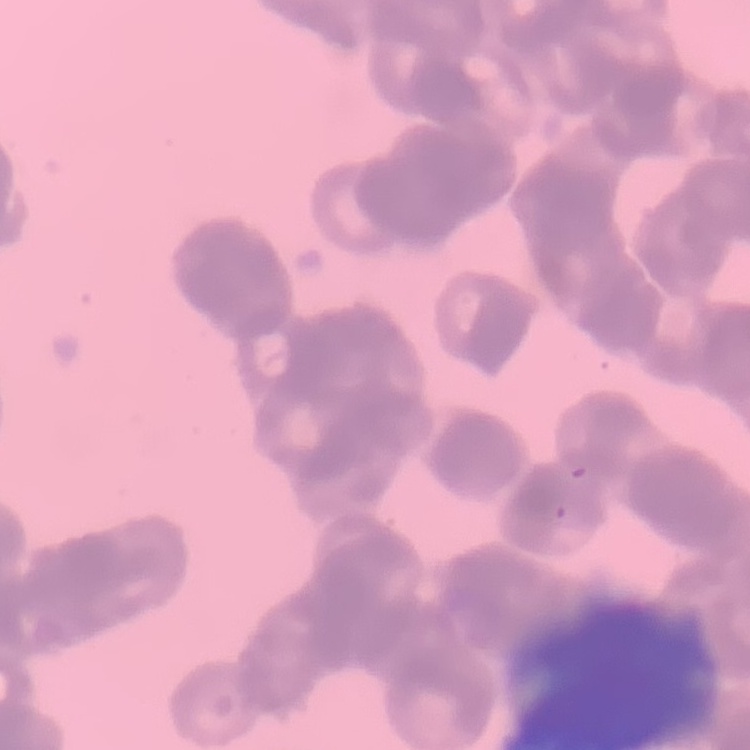
Summary:
  - Red blood cell morphology: rouleaux formation
  - Preparation: thin blood smear
  - Stain: Field's or Giemsa
  - Image type: one tile cut from a larger photomicrograph